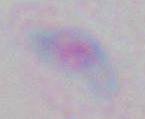

Toxoplasma gondii is seen. 1000x magnification. Micrograph.